Give the position of every Plasmodium parasite visible.
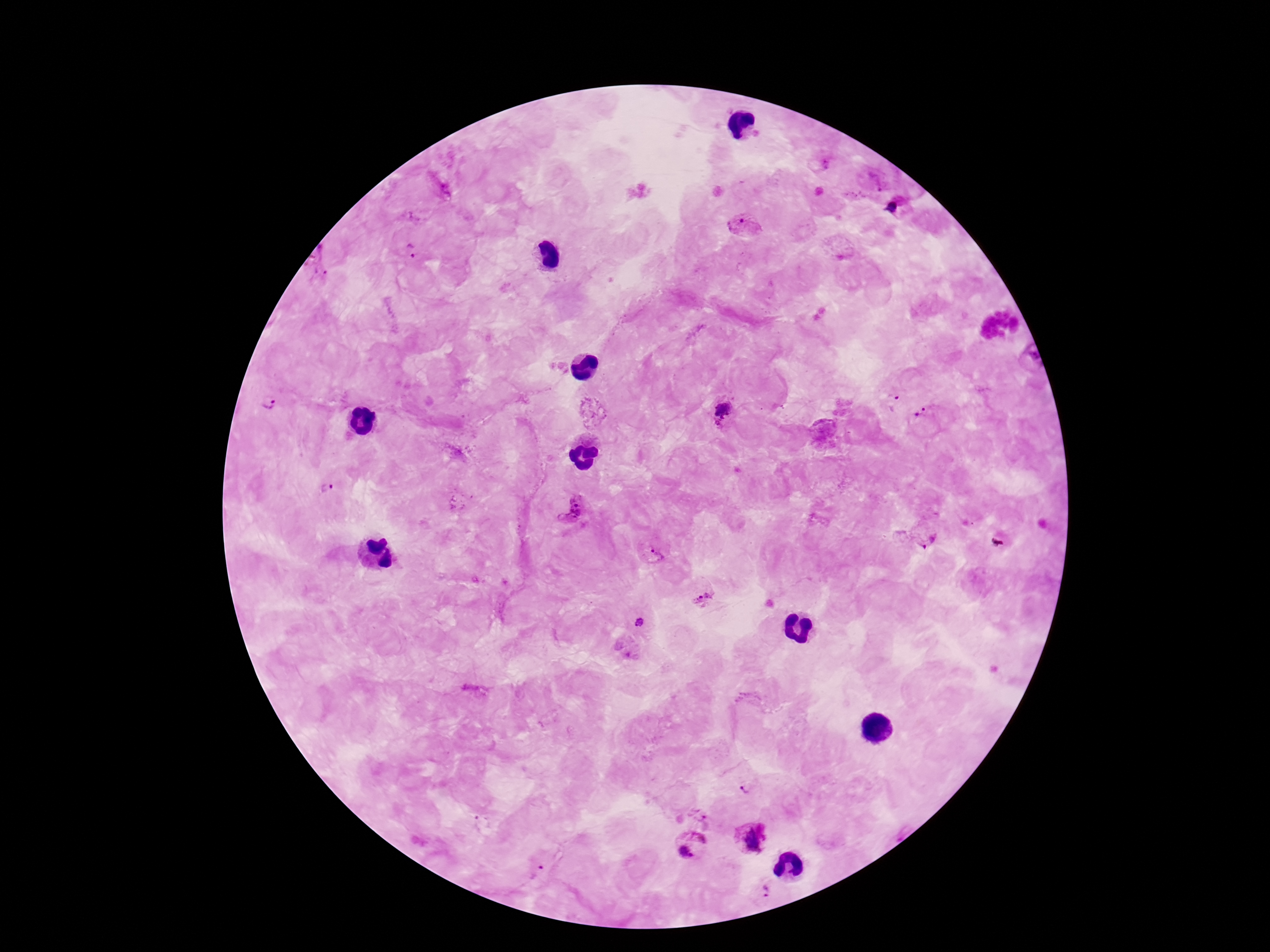

Approximate centers as (x, y) in pixels.
Plasmodium parasites: (830, 164), (876, 180), (444, 190), (892, 207), (739, 226), (411, 252), (321, 264), (892, 401), (268, 404), (726, 411), (923, 417), (327, 488), (567, 506), (925, 537), (655, 553), (701, 596), (639, 622), (744, 787), (701, 812), (750, 838), (692, 845), (536, 870), (761, 890).

preparation = thick blood film
magnification = 100x
capture = smartphone camera through the microscope eyepiece
stain = Giemsa
patient malaria status = positive
image size = 1270×952 pixels
field of view = one from this slide